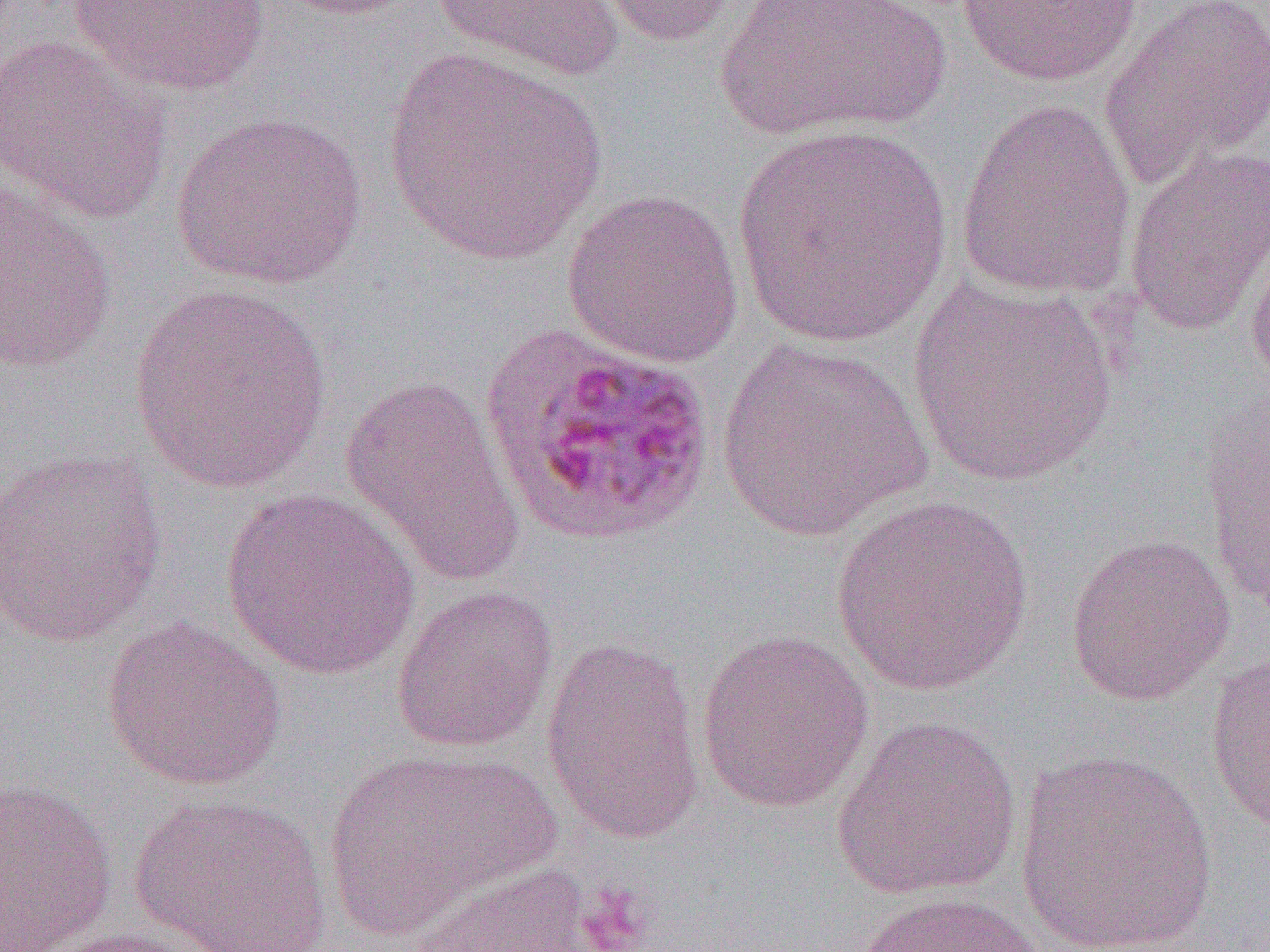

slide-level diagnosis = Plasmodium ovale
image size = 1270×952 pixels
preparation = thin blood smear
uninfected red blood cell locations = approximate bounding boxes as named x1/y1/x2/y2 corners in pixels: (x1=263, y1=0, x2=427, y2=19), (x1=431, y1=0, x2=625, y2=82), (x1=585, y1=0, x2=751, y2=47), (x1=721, y1=0, x2=943, y2=143), (x1=954, y1=0, x2=1146, y2=87), (x1=1098, y1=0, x2=1269, y2=189), (x1=65, y1=1, x2=275, y2=98), (x1=0, y1=35, x2=175, y2=223), (x1=382, y1=49, x2=607, y2=265), (x1=956, y1=98, x2=1136, y2=299), (x1=169, y1=110, x2=369, y2=290), (x1=733, y1=122, x2=953, y2=349), (x1=1122, y1=143, x2=1270, y2=336), (x1=0, y1=176, x2=119, y2=374), (x1=561, y1=188, x2=745, y2=368), (x1=1243, y1=212, x2=1270, y2=396), (x1=909, y1=274, x2=1118, y2=489), (x1=127, y1=284, x2=334, y2=495), (x1=714, y1=338, x2=933, y2=542), (x1=339, y1=374, x2=527, y2=591), (x1=1201, y1=392, x2=1269, y2=616), (x1=0, y1=446, x2=169, y2=647), (x1=221, y1=488, x2=423, y2=680), (x1=831, y1=495, x2=1035, y2=697), (x1=1065, y1=532, x2=1236, y2=705), (x1=390, y1=585, x2=559, y2=753), (x1=101, y1=617, x2=288, y2=792), (x1=696, y1=628, x2=874, y2=813), (x1=541, y1=636, x2=706, y2=845), (x1=1204, y1=652, x2=1270, y2=833), (x1=832, y1=714, x2=1023, y2=901), (x1=321, y1=748, x2=557, y2=940), (x1=1014, y1=750, x2=1220, y2=951), (x1=0, y1=777, x2=119, y2=951), (x1=129, y1=792, x2=333, y2=951), (x1=410, y1=860, x2=607, y2=952), (x1=855, y1=891, x2=1050, y2=952), (x1=28, y1=924, x2=231, y2=952)
field of view = single
magnification = 1000x
modality = light microscopy
platelet locations = approximate bounding boxes as named x1/y1/x2/y2 corners in pixels: (x1=575, y1=879, x2=657, y2=952)